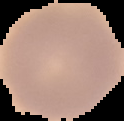

malaria status = uninfected
image type = cell region segmented out of the field of view; surrounding area masked to black
preparation = thin blood smear
image size = 124×121 pixels